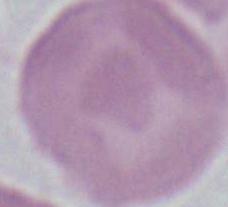
1000x magnification. An erythrocyte is seen. Micrograph.